Give the position of every Plasmodium parasite visible.
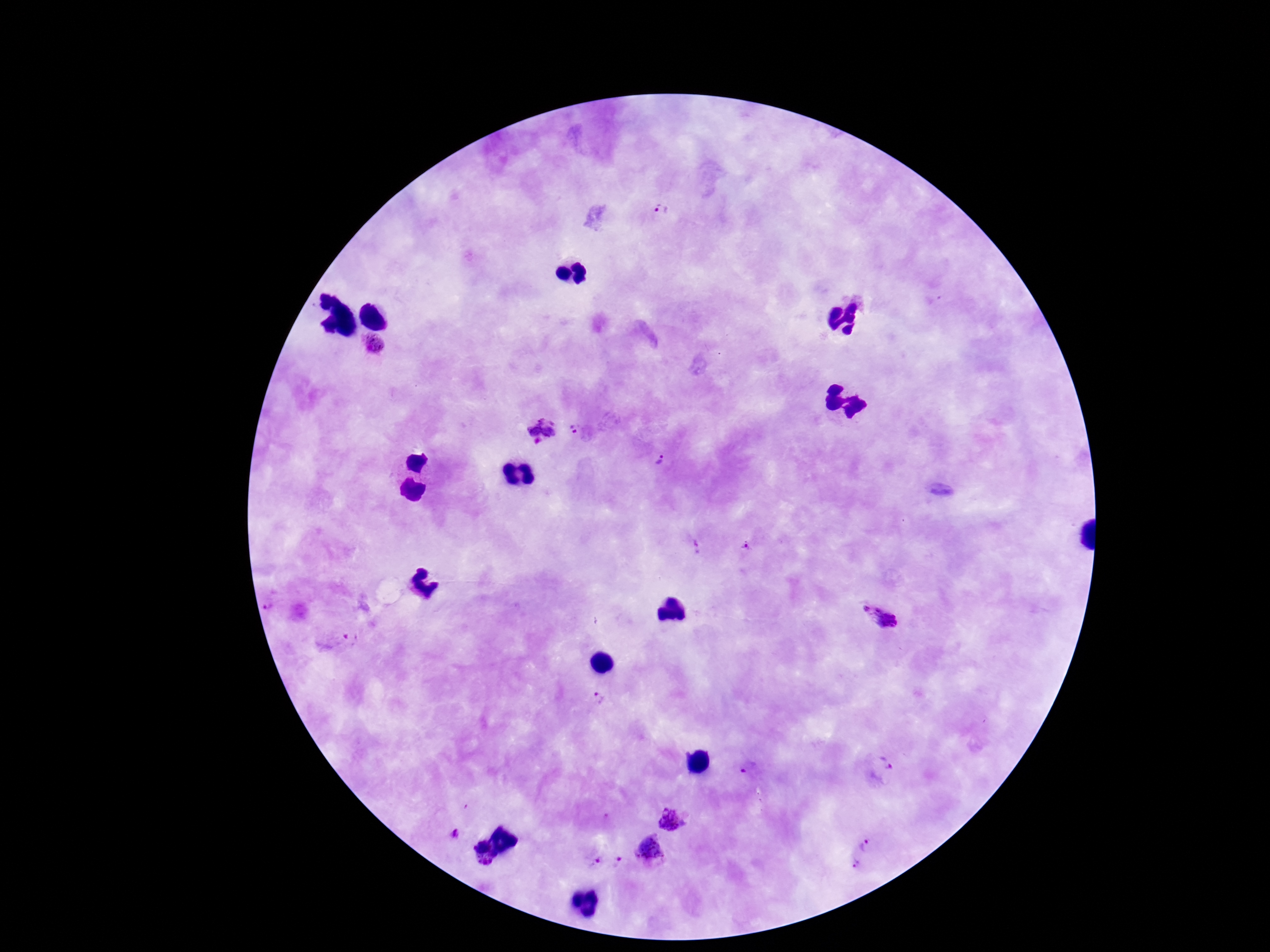

Approximate centers as [x, y] in pixels.
Plasmodium parasites: [659, 208], [377, 343], [576, 430], [541, 431], [664, 460], [746, 547], [271, 606], [878, 617], [599, 703], [884, 763], [748, 768], [670, 819], [455, 834], [865, 846], [650, 848], [480, 852], [617, 860], [854, 864], [594, 865].

100x magnification. Single field of view. Photographed through the microscope eyepiece with a smartphone camera. Patient malaria status: positive. Thick blood film. Image is 1270×952 pixels. Giemsa stain.